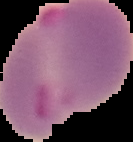

Image is 133×142 pixels. Segmented cell region on a black background. Result: Plasmodium parasites detected. From a thin blood smear.